Comment on the morphology of the red blood cells.
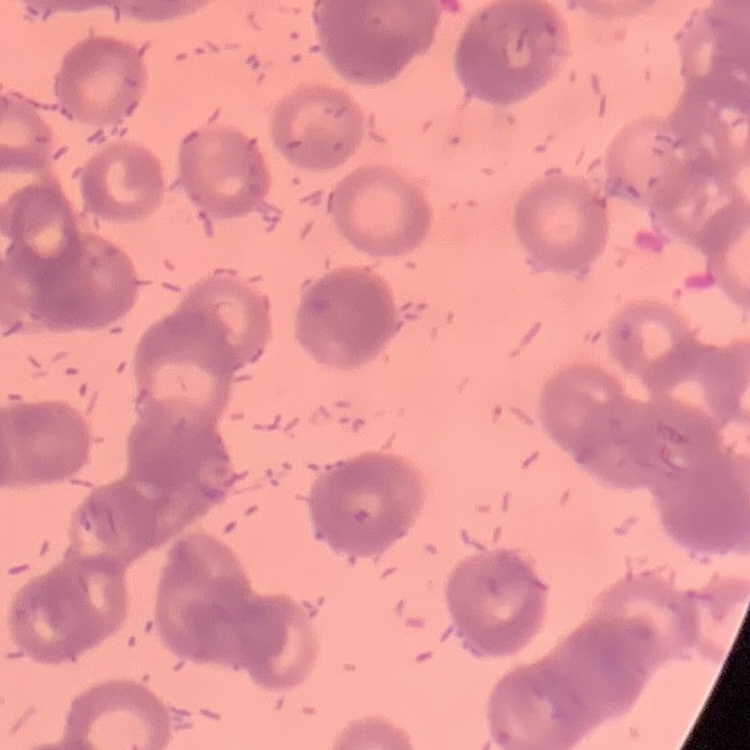
They show rouleaux formation.

Stained with either Field's or Giemsa. Thin peripheral smear. Square crop of a larger photomicrograph.